Report the malaria status of this cell.
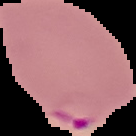

Parasitized.

{
  "image_type": "cell region segmented out of the field of view; surrounding area masked to black",
  "image_size": "136×136 pixels",
  "preparation": "thin blood smear"
}